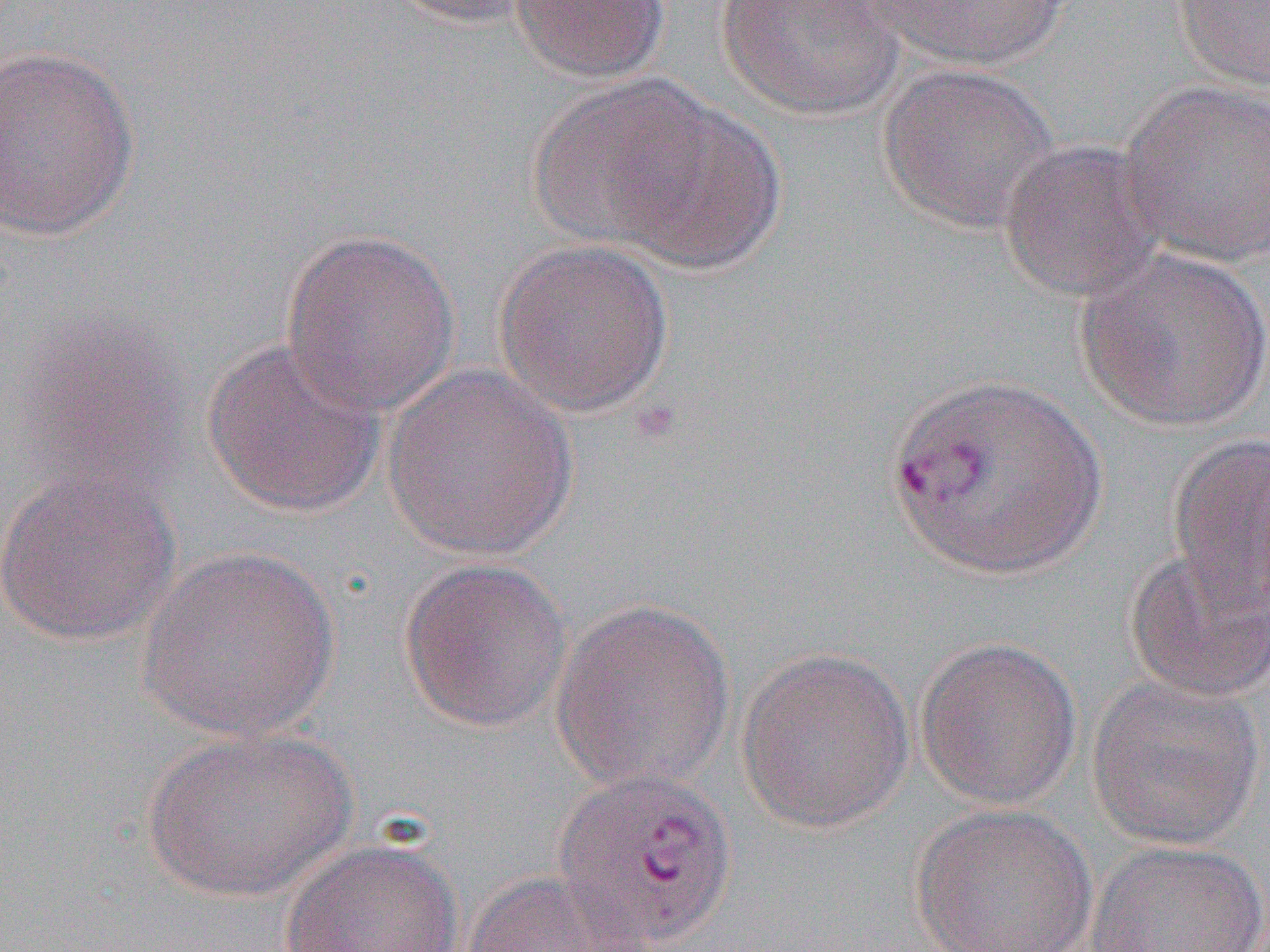

Summary:
  - Coordinate format: approximate bounding boxes as (x1, y1, x2, y2) in pixels
  - Plasmodium vivax-infected red blood cell locations: (551, 767, 740, 948)
  - Uninfected red blood cell locations: (386, 0, 545, 29), (510, 0, 672, 83), (855, 0, 1076, 69), (1170, 0, 1270, 92), (714, 1, 907, 121), (0, 43, 141, 241), (876, 62, 1058, 234), (533, 79, 776, 267), (1118, 80, 1270, 267), (997, 138, 1165, 304), (278, 227, 461, 417), (492, 238, 675, 417), (1076, 246, 1270, 433), (200, 334, 388, 519), (381, 364, 580, 560), (1166, 433, 1270, 616), (0, 462, 181, 648), (137, 544, 340, 741), (1123, 548, 1270, 703), (398, 557, 574, 734), (549, 598, 735, 794), (914, 636, 1082, 810), (736, 646, 914, 833), (1086, 674, 1266, 850), (140, 728, 358, 900), (911, 803, 1098, 952), (279, 837, 464, 952), (1084, 839, 1269, 952), (460, 870, 658, 952)
  - Slide-level diagnosis: Plasmodium vivax
  - Image size: 1270×952 pixels
  - Field of view: one of a larger specimen
  - Modality: optical microscopy
  - Preparation: thin blood smear
  - Magnification: 1000x